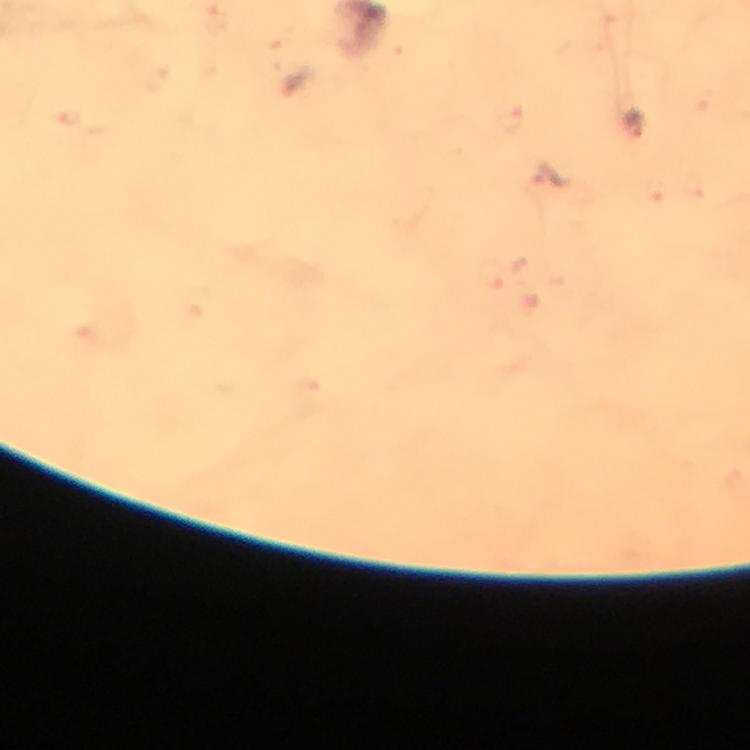

context = from a malaria diagnostic workup
image size = 750×750 pixels
stain = Giemsa
preparation = thick blood film
capture = smartphone mounted on the microscope
cropped from = a single field of view
magnification = 100x
Plasmodium parasite locations = approximate centers as [x, y] in pixels: [635, 125]
immersion oil = applied